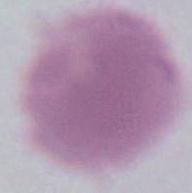 An erythrocyte is shown. 1000x magnification. Photomicrograph.